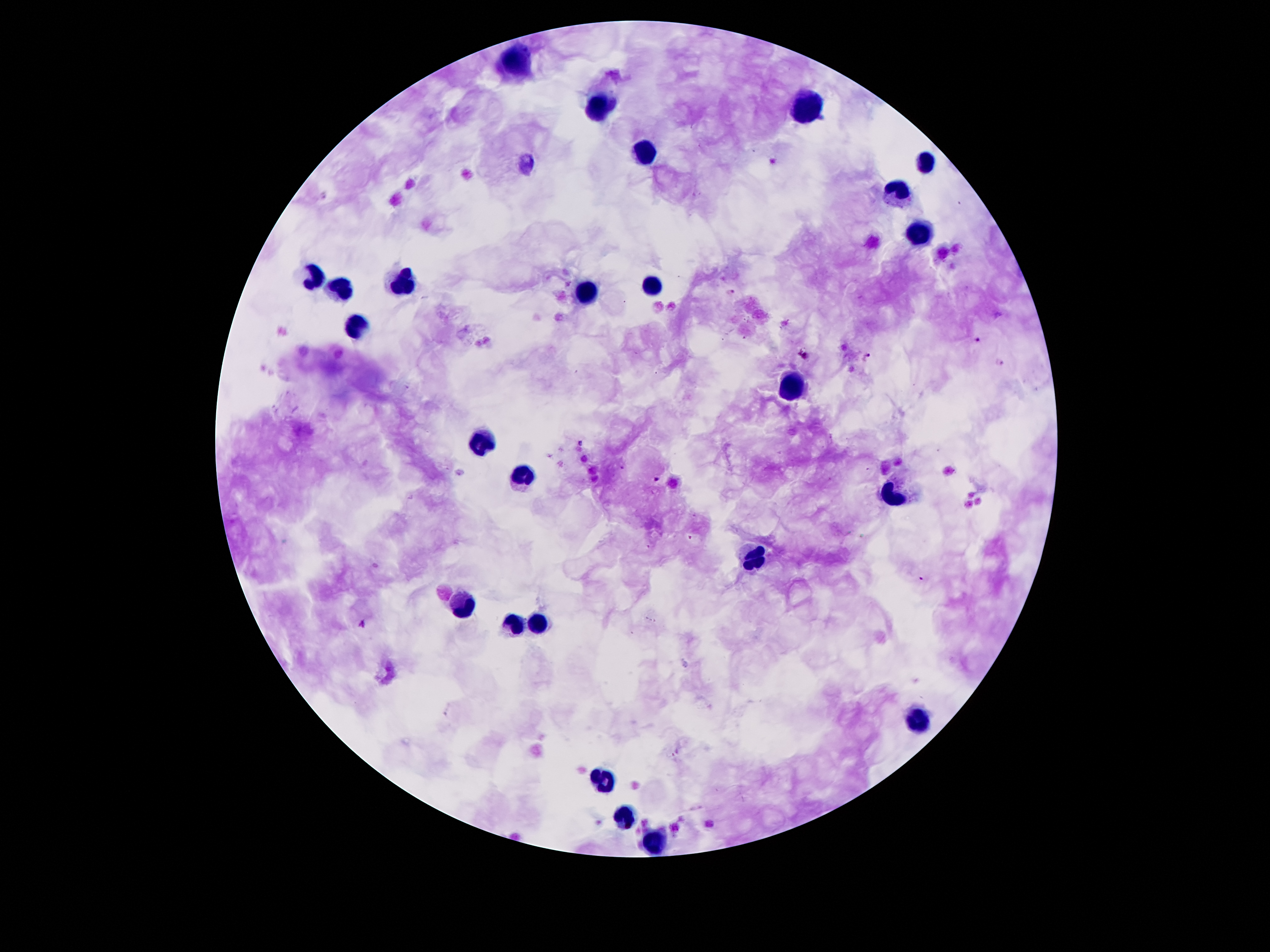
Approximate object centers, in pixels from the top-left corner.
Summary:
  - Malaria parasite locations: (x=732, y=291), (x=978, y=341), (x=805, y=356), (x=866, y=358), (x=999, y=362), (x=580, y=443), (x=657, y=479), (x=922, y=580)
  - Leukocyte locations: (x=516, y=60), (x=806, y=104), (x=598, y=107), (x=648, y=150), (x=926, y=161), (x=897, y=194), (x=920, y=236), (x=312, y=275), (x=654, y=284), (x=401, y=285), (x=341, y=290), (x=589, y=292), (x=356, y=325), (x=789, y=389), (x=480, y=436), (x=890, y=494), (x=757, y=556), (x=462, y=605), (x=535, y=626), (x=513, y=627), (x=917, y=723), (x=604, y=782), (x=624, y=817), (x=657, y=840)
  - Image size: 1270×952 pixels
  - Capture: smartphone through the microscope eyepiece
  - Magnification: 100x
  - Preparation: thick blood smear
  - Patient malaria status: infected with Plasmodium falciparum
  - Field of view: single
  - Stain: Giemsa